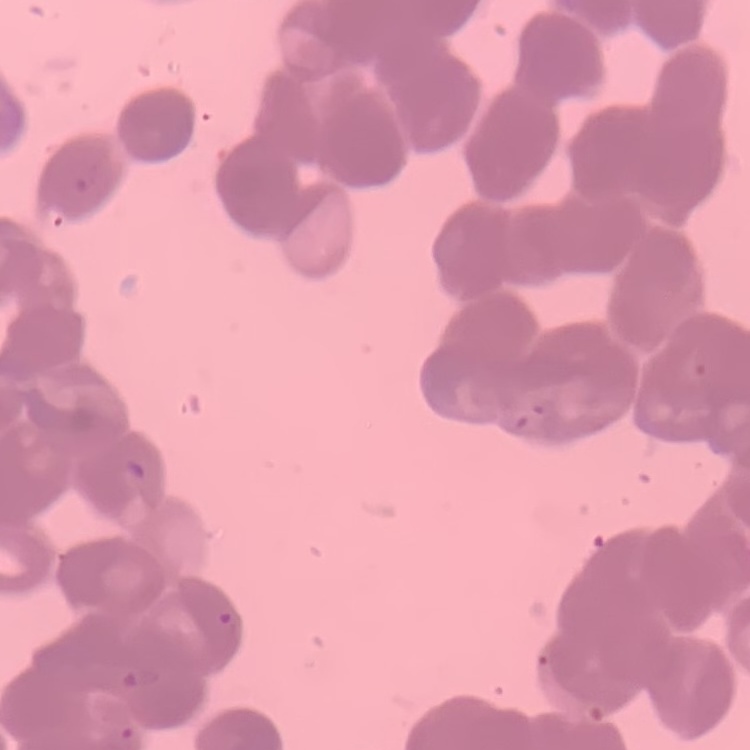
Summary:
  - Erythrocyte morphology: rouleaux formation
  - Image type: square crop of a larger photomicrograph
  - Preparation: thin blood film
  - Stain: Field's or Giemsa